Name the parasite shown.
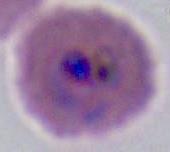

Plasmodium.

Captured at either 400x or 1000x magnification. Photomicrograph.